Classify this cell by malaria status.
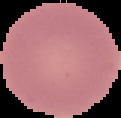

It is uninfected.

preparation = thin blood film
image type = cell region segmented out of the field of view; surrounding area masked to black
image size = 121×118 pixels